Report the malaria status of this cell.
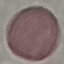
It is uninfected.

Summary:
  - Preparation: thin smear
  - Stain: Giemsa
  - Capture: smartphone through the microscope eyepiece
  - Image type: automatically extracted cell patch, resized to 64 × 64 pixels